Give the position of every leukocyte visible.
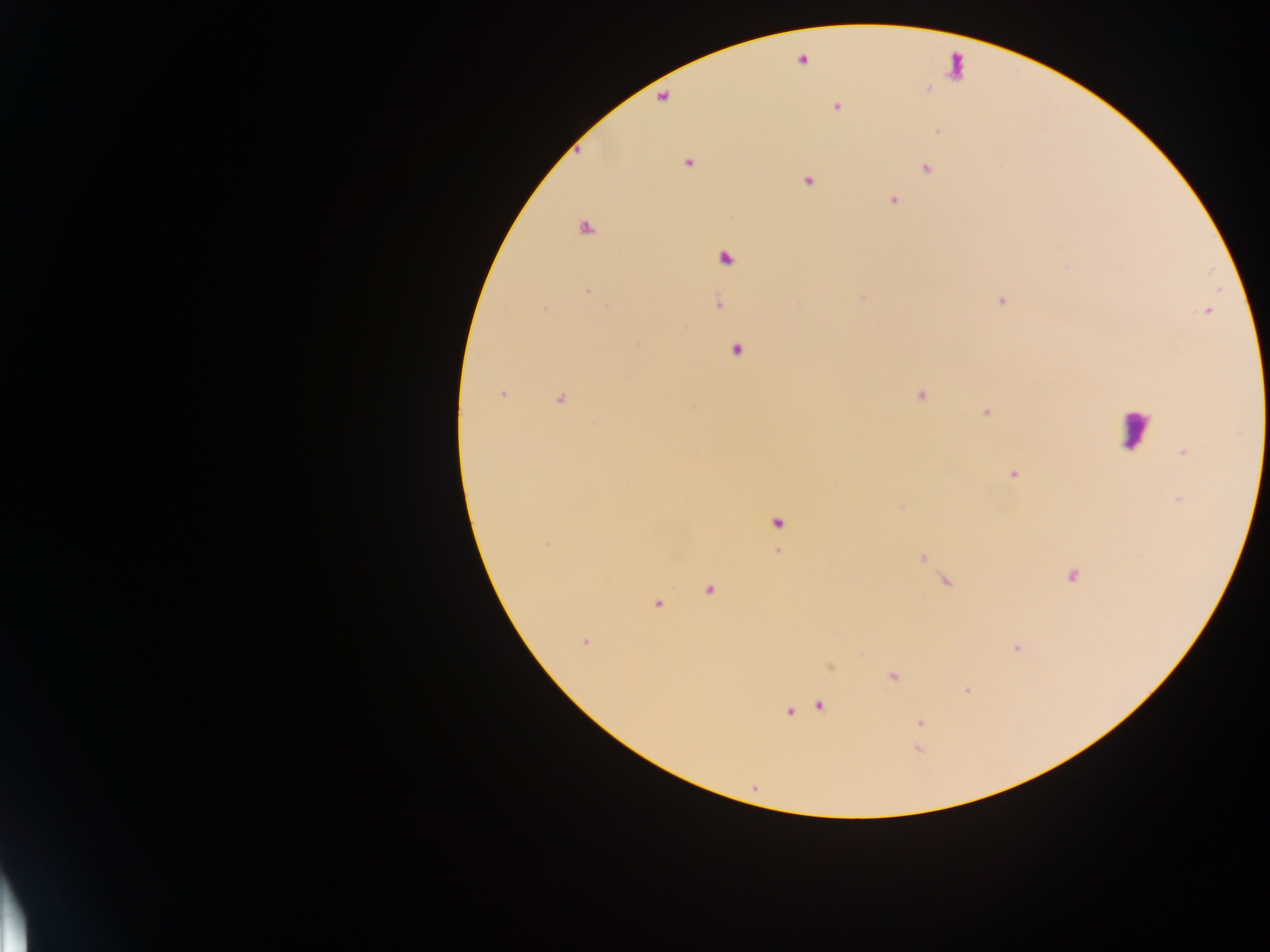
Approximate centers as x y in pixels.
Leukocytes: 1135 429.

Summary:
  - Plasmodium parasite locations: 803 60; 837 107; 687 163; 925 169; 808 181; 892 199; 725 258; 587 291; 1002 301; 718 303; 544 309; 638 343; 735 350; 502 394; 921 396; 560 400; 986 412; 1183 452; 1012 475; 777 522; 547 544; 778 551; 922 558; 1072 576; 947 581; 709 590; 657 605; 585 642; 1017 648; 892 676; 967 690; 820 706; 789 711; 920 723
  - Preparation: thick blood film
  - Capture: mobile-phone photograph through a microscope
  - Field of view: single
  - Image size: 1270×952 pixels
  - Country: Ghana